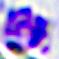
Summary:
  - Modality: micrograph
  - Identification: leukocyte
  - Magnification: 400x